Name the parasite shown.
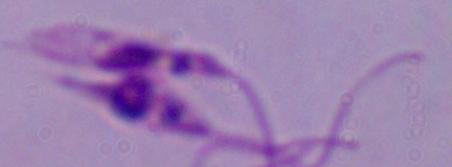
This is Leishmania.

modality = micrograph
magnification = 1000x